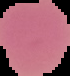

Result: no Plasmodium parasites detected. From a thin blood smear. The area outside the segmented cell region is set to black. Image is 70×76 pixels.